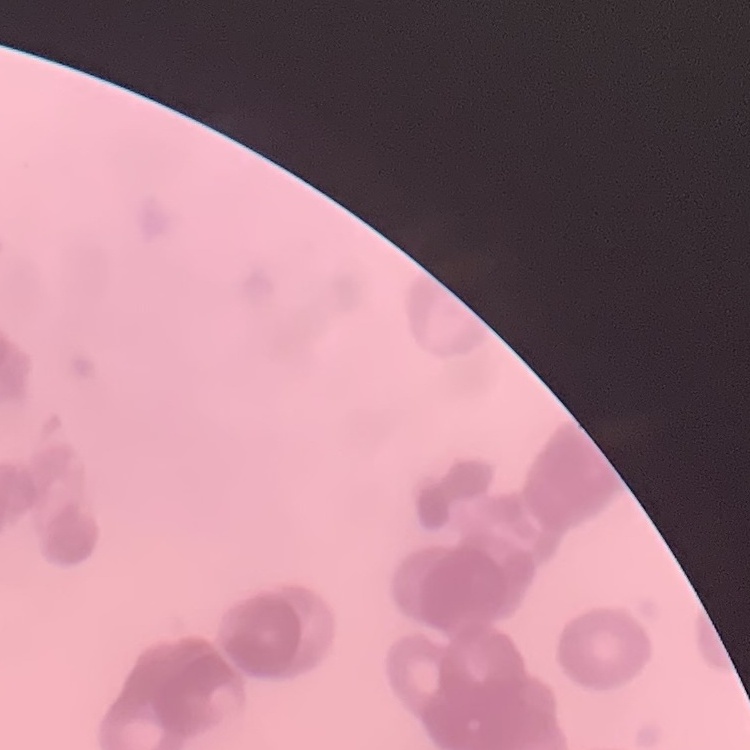
Summary:
  - Erythrocyte morphology: rouleaux formation
  - Stain: Field's or Giemsa
  - Preparation: thin blood smear
  - Image type: one tile cut from a larger photomicrograph